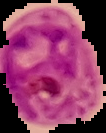

Image is 106×133 pixels. Segmented cell region on a black background. From a thin blood film. Result: malaria parasites identified.